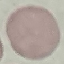
Summary:
  - Result: no malaria parasites seen
  - Image type: cell patch, automatically extracted from a larger field of view and resized to 64 × 64 pixels
  - Preparation: thin blood smear
  - Stain: Giemsa
  - Capture: smartphone camera at the microscope eyepiece